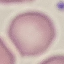

Summary:
  - Malaria status: uninfected
  - Stain: Giemsa
  - Image type: cell patch, automatically extracted from a larger field of view and resized to 64 × 64 pixels
  - Capture: smartphone through the microscope eyepiece
  - Preparation: thin blood film